Report the malaria status of this cell.
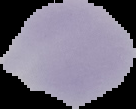
It is uninfected.

From a thin blood smear. The area outside the segmented cell region is set to black. Image is 136×109 pixels.